Name the parasite shown.
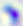

This is Toxoplasma gondii.

Summary:
  - Magnification: 400x
  - Modality: micrograph